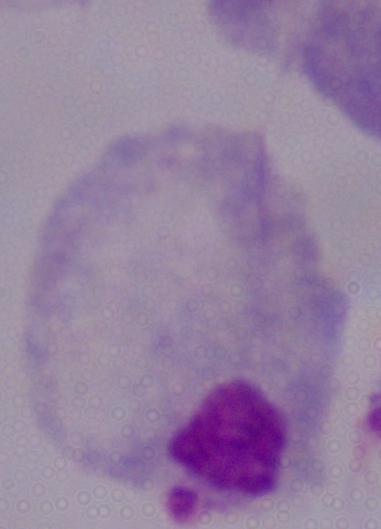

1000x magnification. A trichomonad is seen. Photomicrograph.